Assess this cell for malaria.
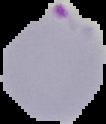
It is parasitized.

Segmented cell region on a black background. Image is 106×124 pixels. From a thin blood film.